Locate and identify every blood parasite.
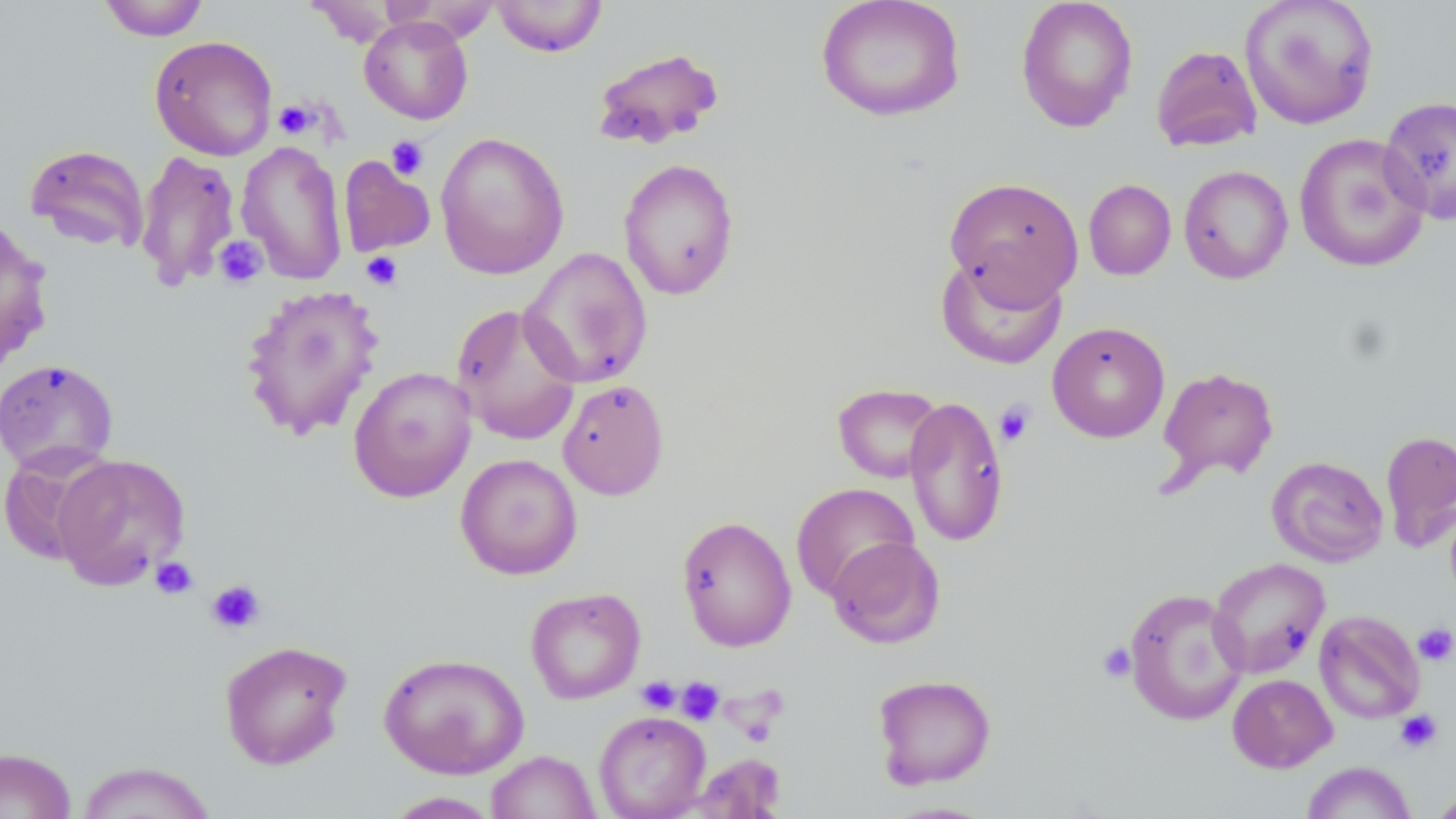
No blood parasites seen.

Summary:
  - Coordinate format: approximate bounding boxes as (x1,y1)-(x2,y2) corner pairs in pixels
  - Uninfected red blood cell locations: (97,0)-(210,41), (492,0)-(609,57), (815,0)-(966,122), (1016,0)-(1138,133), (1239,0)-(1380,130), (359,16)-(473,124), (149,36)-(278,161), (1151,45)-(1262,152), (591,47)-(725,151), (1379,96)-(1456,224), (434,132)-(570,280), (1294,132)-(1431,273), (236,139)-(349,285), (24,143)-(150,253), (135,149)-(241,290), (338,156)-(435,258), (618,157)-(740,301), (1179,165)-(1293,283), (944,176)-(1084,306), (1084,179)-(1177,280), (0,215)-(54,375), (519,247)-(653,389), (935,253)-(1067,370), (239,283)-(385,441), (450,303)-(583,446), (1047,321)-(1170,443), (0,358)-(119,476), (348,366)-(477,503), (1157,366)-(1279,486), (557,379)-(669,499), (832,382)-(945,484), (903,395)-(1009,547), (1380,429)-(1456,553), (0,446)-(115,566), (51,453)-(191,590), (455,453)-(583,580), (1267,456)-(1388,567), (791,482)-(919,600), (676,515)-(797,652), (826,536)-(946,649), (1207,557)-(1330,678), (525,586)-(646,705), (1123,588)-(1248,726), (1314,610)-(1424,724), (218,640)-(353,770), (378,651)-(530,778), (872,673)-(997,789), (1227,674)-(1337,773), (593,710)-(711,819), (0,747)-(77,819), (486,750)-(600,818), (689,754)-(786,818), (74,761)-(218,818), (1300,761)-(1416,819), (1426,788)-(1455,818), (382,791)-(502,818)
  - Platelet locations: (274,100)-(319,139), (386,136)-(429,180), (212,236)-(268,288), (361,251)-(403,290), (995,401)-(1036,446), (150,557)-(198,599), (206,579)-(266,634), (1412,622)-(1456,668), (1097,642)-(1137,683), (637,676)-(681,714), (676,677)-(725,726), (1395,709)-(1443,753)
  - Slide-level diagnosis: negative for blood parasites
  - Preparation: thin blood film
  - Image size: 1456×819 pixels
  - Magnification: 1000x
  - Stain: May-Grünwald-Giemsa
  - Modality: light microscopy
  - Field of view: one of a larger specimen